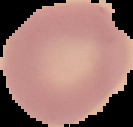
Summary:
  - Image size: 133×127 pixels
  - Preparation: thin blood smear
  - Image type: segmented cell region on a black background
  - Malaria status: uninfected